Locate every Plasmodium parasite.
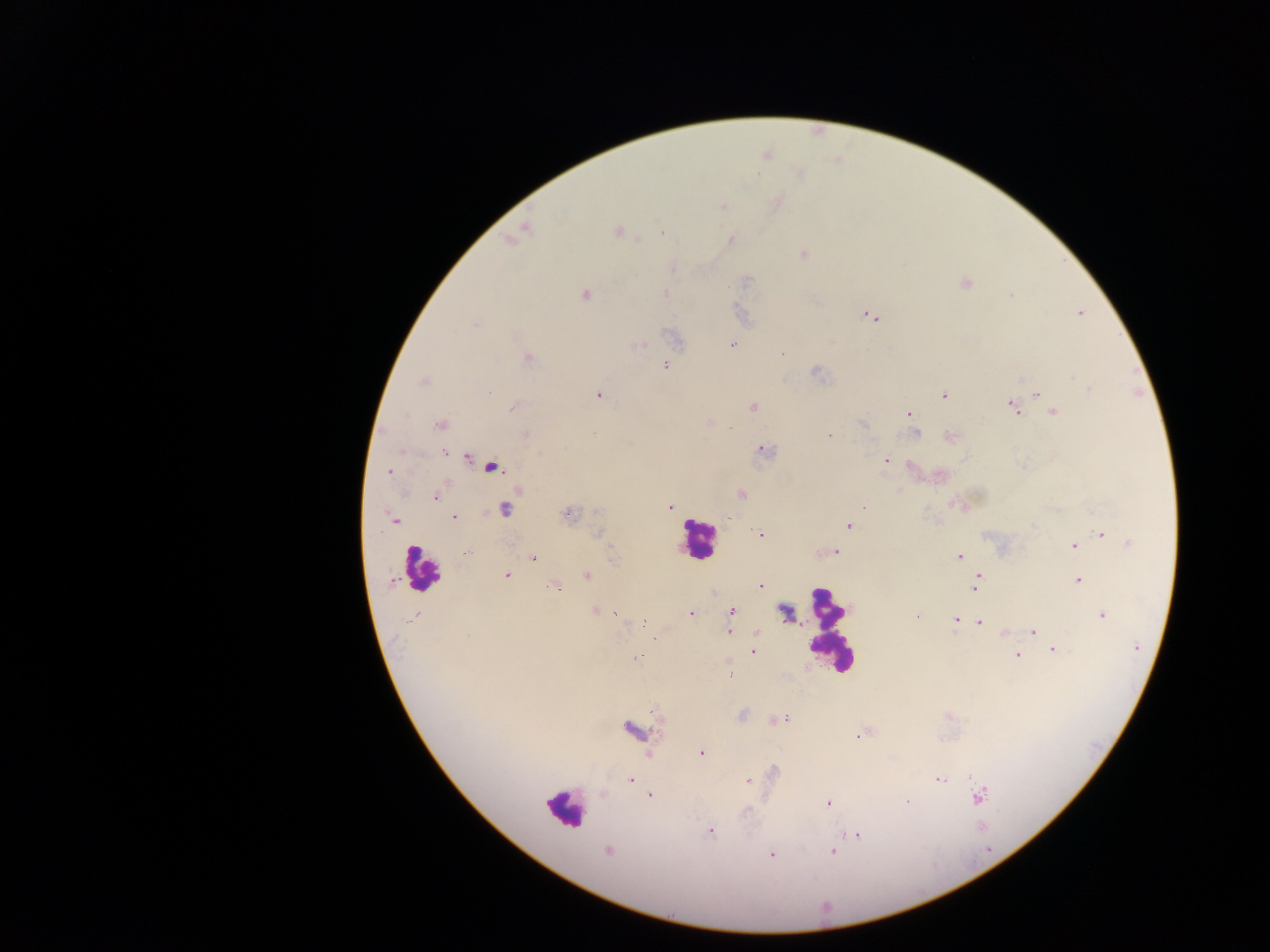
Approximate centers as x y in pixels.
Plasmodium parasites: 724 207; 617 231; 639 240; 731 240; 803 254; 672 268; 747 280; 964 284; 665 293; 1010 294; 585 295; 1080 312; 870 316; 475 323; 732 344; 782 354; 527 358; 665 366; 815 371; 423 381; 1090 389; 1038 393; 598 395; 944 396; 1047 404; 753 407; 1013 407; 511 408; 1053 412; 908 413; 863 424; 440 425; 913 428; 917 432; 592 434; 525 435; 828 435; 951 436; 762 450; 444 453; 541 453; 466 458; 886 460; 491 466; 390 472; 741 493; 435 498; 669 507; 863 507; 504 510; 567 513; 454 517; 729 517; 394 521; 848 525; 1033 526; 1101 533; 598 534; 761 534; 1130 543; 1074 546; 836 551; 467 552; 959 556; 533 558; 507 576; 588 576; 978 578; 1078 580; 392 582; 760 586; 976 586; 556 588; 595 611; 732 611; 691 613; 616 614; 1102 615; 413 616; 917 617; 956 619; 645 622; 980 622; 1033 631; 729 632; 1004 633; 1136 647; 1053 650; 753 651; 1017 655; 637 658; 730 676; 784 719; 777 720; 631 729; 858 735; 701 753; 630 779; 939 779; 747 781; 651 795; 980 797; 827 802; 906 802; 710 831; 857 834; 608 851; 832 851; 772 855.

field of view = single
leukocyte locations = approximate centers as x y in pixels: 697 540; 422 570; 830 629; 565 808
capture = mobile-phone photograph through a microscope
preparation = thick blood smear
country = Ghana
image size = 1270×952 pixels